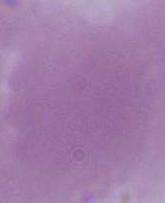
identification = erythrocyte
modality = micrograph
magnification = 1000x